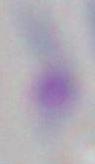
Summary:
  - Modality: micrograph
  - Magnification: 1000x
  - Identification: Toxoplasma gondii